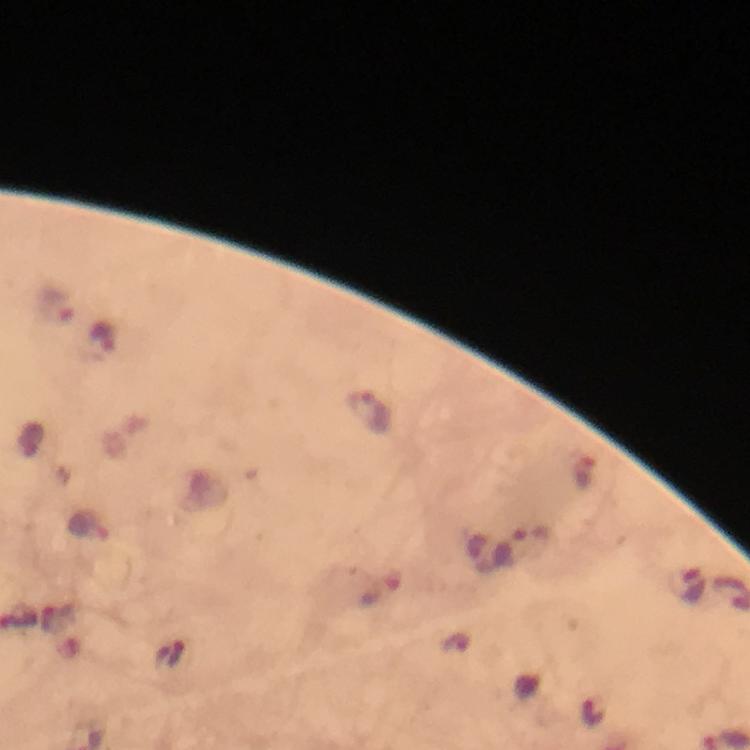
{
  "magnification": "100x",
  "malaria_parasite_locations": "approximate centers as {x, y} in pixels: {57, 305}, {102, 342}, {369, 413}, {584, 474}, {88, 525}, {533, 534}, {689, 587}, {379, 589}, {594, 712}",
  "preparation": "thick blood film",
  "capture": "smartphone photograph through a microscope",
  "stain": "Giemsa",
  "immersion_oil": "used",
  "cropped_from": "a single field of view",
  "image_size": "750×750 pixels",
  "context": "from a malaria diagnostic workup"
}